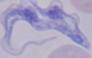

modality = micrograph
identification = trypanosome
magnification = 1000x